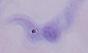

Summary:
  - Modality: photomicrograph
  - Magnification: 1000x
  - Identification: trypanosome